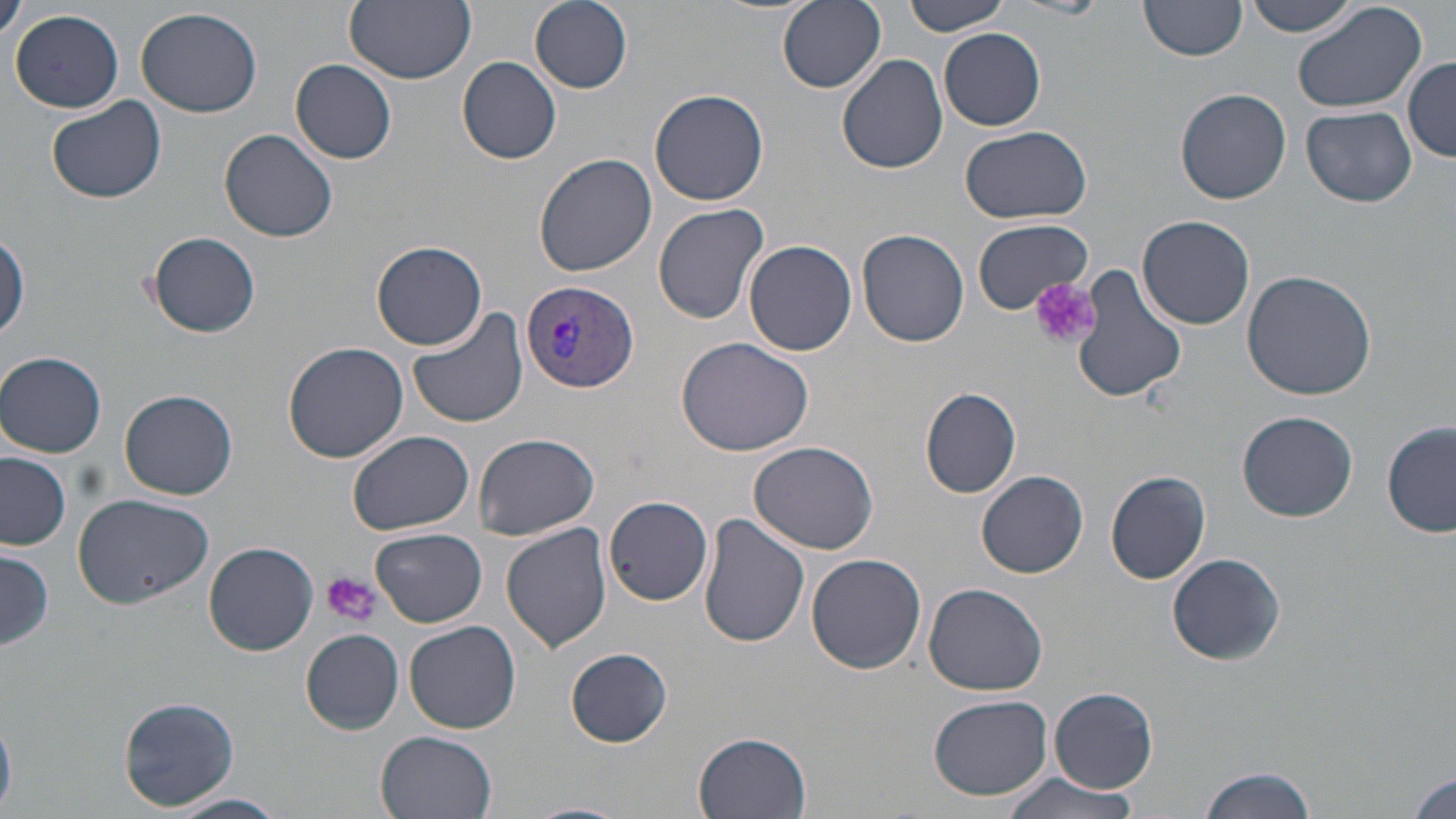
slide-level diagnosis = Plasmodium vivax
image size = 1456×819 pixels
stain = May-Grünwald-Giemsa
field of view = one of a larger specimen
preparation = thin blood smear
uninfected red blood cell locations = approximate bounding boxes as (x1, y1, x2, y2) in pixels: (344, 0, 476, 84), (777, 0, 885, 93), (902, 0, 1014, 37), (1014, 0, 1111, 19), (1291, 0, 1425, 113), (0, 1, 27, 46), (1242, 1, 1363, 37), (529, 2, 634, 93), (1138, 2, 1246, 64), (135, 5, 262, 118), (11, 9, 125, 113), (938, 28, 1046, 131), (838, 54, 950, 174), (457, 56, 562, 165), (1404, 56, 1455, 161), (290, 59, 398, 164), (1174, 88, 1292, 205), (649, 89, 771, 207), (47, 97, 167, 205), (1301, 105, 1418, 207), (960, 126, 1095, 225), (219, 128, 339, 242), (533, 152, 656, 279), (654, 203, 769, 325), (1137, 215, 1255, 330), (972, 218, 1090, 313), (857, 229, 970, 348), (146, 231, 261, 338), (1, 232, 28, 344), (743, 240, 857, 356), (372, 241, 487, 351), (1067, 268, 1188, 403), (1240, 270, 1377, 400), (408, 310, 529, 430), (677, 335, 816, 457), (284, 342, 409, 464), (1, 351, 107, 457), (919, 384, 1022, 499), (119, 390, 238, 500), (1239, 411, 1360, 522), (1383, 420, 1456, 539), (346, 430, 476, 532), (472, 434, 602, 540), (747, 439, 878, 553), (0, 453, 72, 550), (1106, 470, 1212, 585), (976, 471, 1089, 577), (71, 492, 216, 609), (603, 496, 714, 606), (698, 513, 810, 649), (500, 521, 614, 652), (373, 527, 487, 629), (203, 541, 318, 656), (0, 548, 54, 653), (1168, 552, 1287, 665), (807, 554, 927, 676), (923, 582, 1048, 696), (405, 619, 522, 734), (300, 629, 404, 734), (565, 648, 673, 747), (1048, 685, 1159, 794), (929, 694, 1053, 802), (119, 696, 240, 811), (376, 731, 499, 819), (694, 731, 813, 818), (1199, 765, 1314, 819), (1408, 770, 1455, 815), (999, 771, 1145, 819), (167, 793, 288, 819), (519, 800, 629, 819)
platelet locations = approximate bounding boxes as (x1, y1, x2, y2) in pixels: (1029, 278, 1102, 350), (321, 572, 380, 627)
Plasmodium vivax-infected red blood cell locations = approximate bounding boxes as (x1, y1, x2, y2) in pixels: (517, 281, 641, 393)
modality = optical microscopy
magnification = 1000x